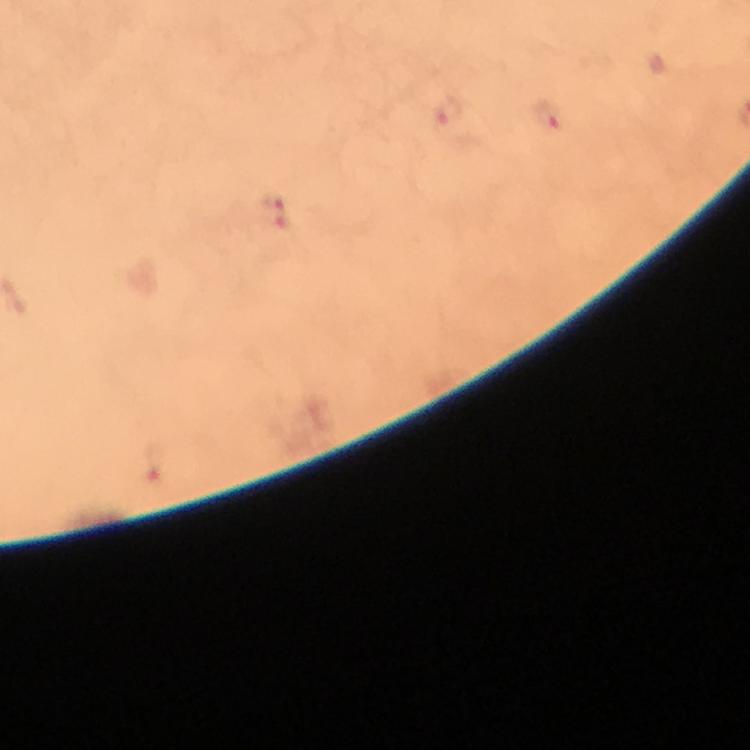 Approximate centers as (x, y) in pixels. Malaria parasite locations: (447, 112), (547, 117), (270, 214), (157, 462). Immersion oil was used. Giemsa-stained preparation. Photographed with a smartphone mounted on the microscope. Image is 750×750 pixels. From a diagnostic examination for malaria. At 100x magnification. Cropped region of a single field of view. Thick smear.